Report the malaria status of this cell.
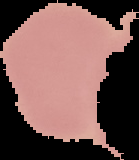
It is uninfected.

image type = segmented cell region with the area outside set to black
preparation = thin blood film
image size = 139×160 pixels